Locate and identify every blood parasite.
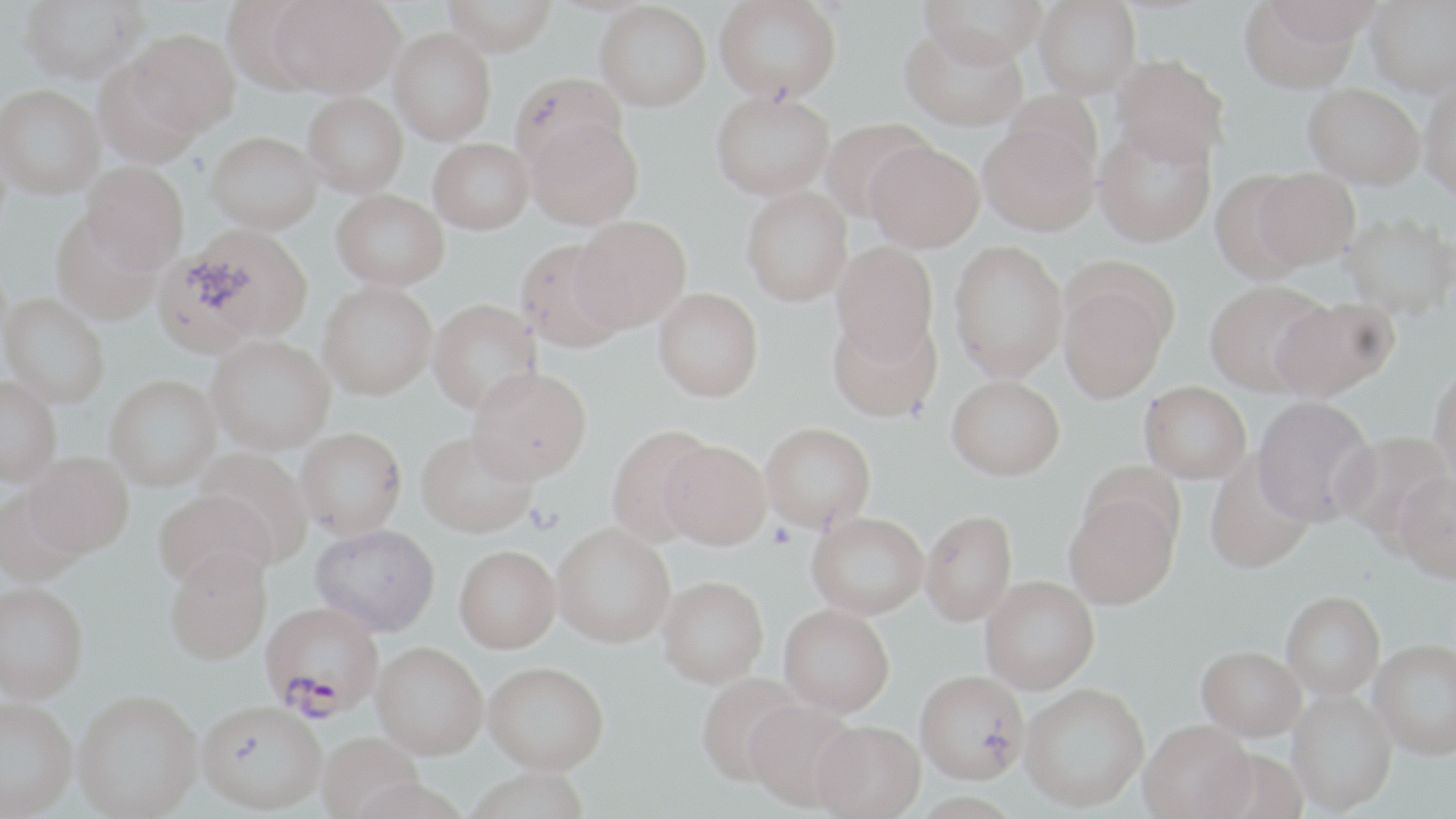
Approximate bounding boxes as (x1,y1)-(x2,y2) corner pairs in pixels.
Plasmodium falciparum-infected red blood cells: (260,605)-(383,724).
No Plasmodium ovale, Plasmodium malariae, Plasmodium vivax, Babesia divergens, or Trypanosoma brucei observed.

Uninfected red blood cell locations: (19,0)-(149,83), (220,0)-(330,94), (272,0)-(403,97), (443,0)-(557,55), (713,0)-(842,103), (920,0)-(1047,68), (1033,0)-(1141,99), (1261,0)-(1383,53), (595,1)-(711,111), (1365,1)-(1456,101), (1238,2)-(1363,99), (900,25)-(1027,132), (389,28)-(496,145), (127,29)-(240,136), (93,57)-(203,168), (1111,57)-(1230,172), (511,70)-(626,174), (1,84)-(104,199), (1419,87)-(1456,207), (1302,88)-(1425,195), (711,90)-(835,200), (302,91)-(408,197), (525,116)-(643,231), (818,118)-(936,223), (979,124)-(1099,241), (1093,128)-(1217,251), (207,130)-(323,234), (428,138)-(534,234), (866,146)-(985,257), (81,161)-(189,273), (1251,171)-(1361,277), (1207,173)-(1316,287), (331,188)-(449,290), (741,188)-(853,310), (50,210)-(163,326), (1341,217)-(1456,325), (572,218)-(690,335), (159,226)-(313,353), (515,240)-(629,355), (831,244)-(939,366), (948,244)-(1068,387), (1057,269)-(1176,406), (317,283)-(437,403), (1204,284)-(1330,400), (652,292)-(764,408), (2,293)-(109,409), (427,300)-(543,419), (1272,300)-(1399,406), (827,313)-(942,426), (206,335)-(336,458), (1429,369)-(1456,489), (467,372)-(592,491), (0,376)-(61,487), (105,376)-(221,491), (946,380)-(1065,486), (1139,385)-(1251,487), (1250,399)-(1378,532), (761,427)-(876,537), (606,428)-(715,549), (294,431)-(407,544), (1337,432)-(1454,545), (415,436)-(536,543), (659,446)-(771,555), (195,449)-(312,562), (24,452)-(133,559), (1203,456)-(1316,577), (1392,476)-(1456,588), (0,487)-(86,588), (154,491)-(275,594), (1065,492)-(1181,614), (921,514)-(1018,630), (806,516)-(928,623), (310,527)-(440,641), (552,529)-(675,653), (453,550)-(562,657), (164,556)-(272,670), (980,580)-(1100,698), (657,581)-(768,693), (0,582)-(89,706), (1282,595)-(1385,702), (777,609)-(894,721), (1369,643)-(1456,763), (371,647)-(488,765), (1196,650)-(1306,746), (482,667)-(609,781), (696,675)-(807,791), (915,675)-(1028,789), (1019,688)-(1149,815), (1286,692)-(1398,817), (73,695)-(202,819), (0,699)-(78,819), (744,703)-(863,816), (196,706)-(327,818), (1139,723)-(1256,819), (811,725)-(925,819), (318,736)-(425,819), (1205,752)-(1308,819), (467,772)-(589,819), (350,782)-(469,819), (911,796)-(1022,819). Platelet locations: (767,523)-(797,550). Slide-level diagnosis: Plasmodium falciparum. Image is 1456×819 pixels. One field of a larger specimen. Optical microscopy. May-Grünwald-Giemsa stain. Thin blood smear. Captured at 1000x magnification.